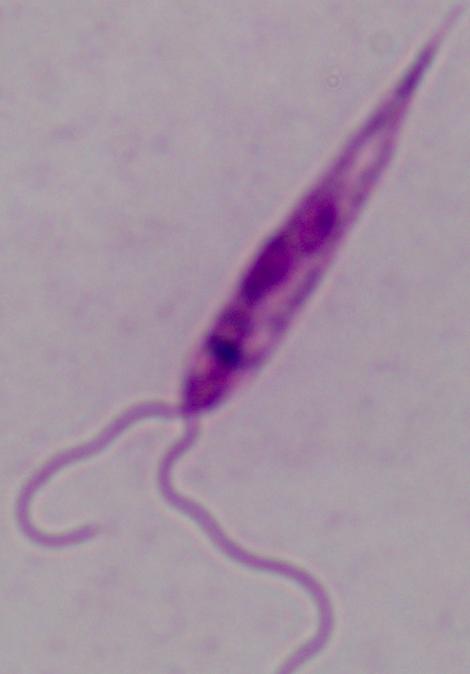
Summary:
  - Identification: Leishmania
  - Magnification: 1000x
  - Modality: photomicrograph